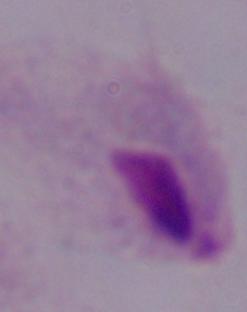

Summary:
  - Identification: trichomonad
  - Modality: micrograph
  - Magnification: 1000x